Assess this cell for malaria.
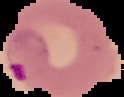

Parasitized.

{
  "preparation": "thin blood film",
  "image_size": "124×97 pixels",
  "image_type": "segmented cell region on a black background"
}